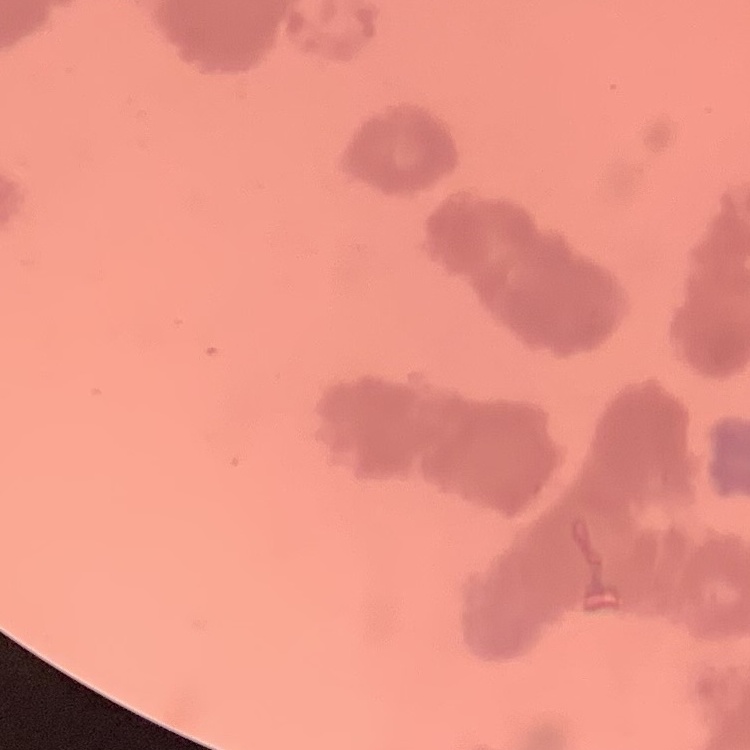
red_blood_cell_morphology: rouleaux formation
preparation: thin peripheral smear
stain: Field's or Giemsa
image_type: one tile cut from a larger photomicrograph